Describe the morphology of the erythrocytes.
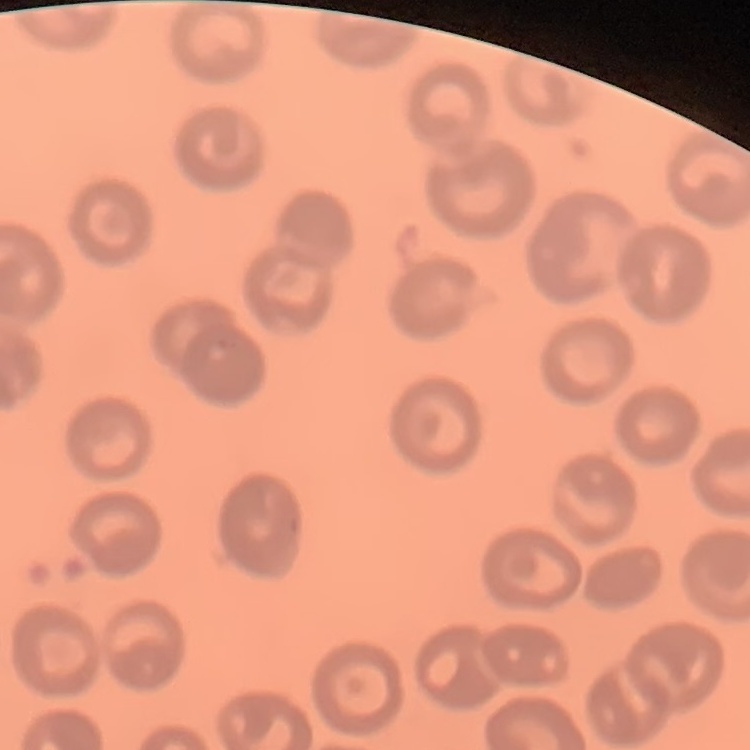

No rouleaux formation.

Summary:
  - Image type: one tile cut from a larger photomicrograph
  - Preparation: thin peripheral smear
  - Stain: Field's or Giemsa